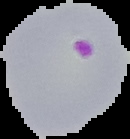

image size = 130×139 pixels
image type = segmented cell region with the area outside set to black
malaria status = parasitized
preparation = thin blood film